State which cell type is depicted.
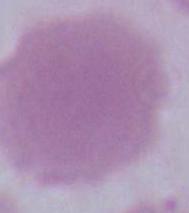
This is an erythrocyte.

Summary:
  - Modality: photomicrograph
  - Magnification: 1000x